Name the blood parasite species.
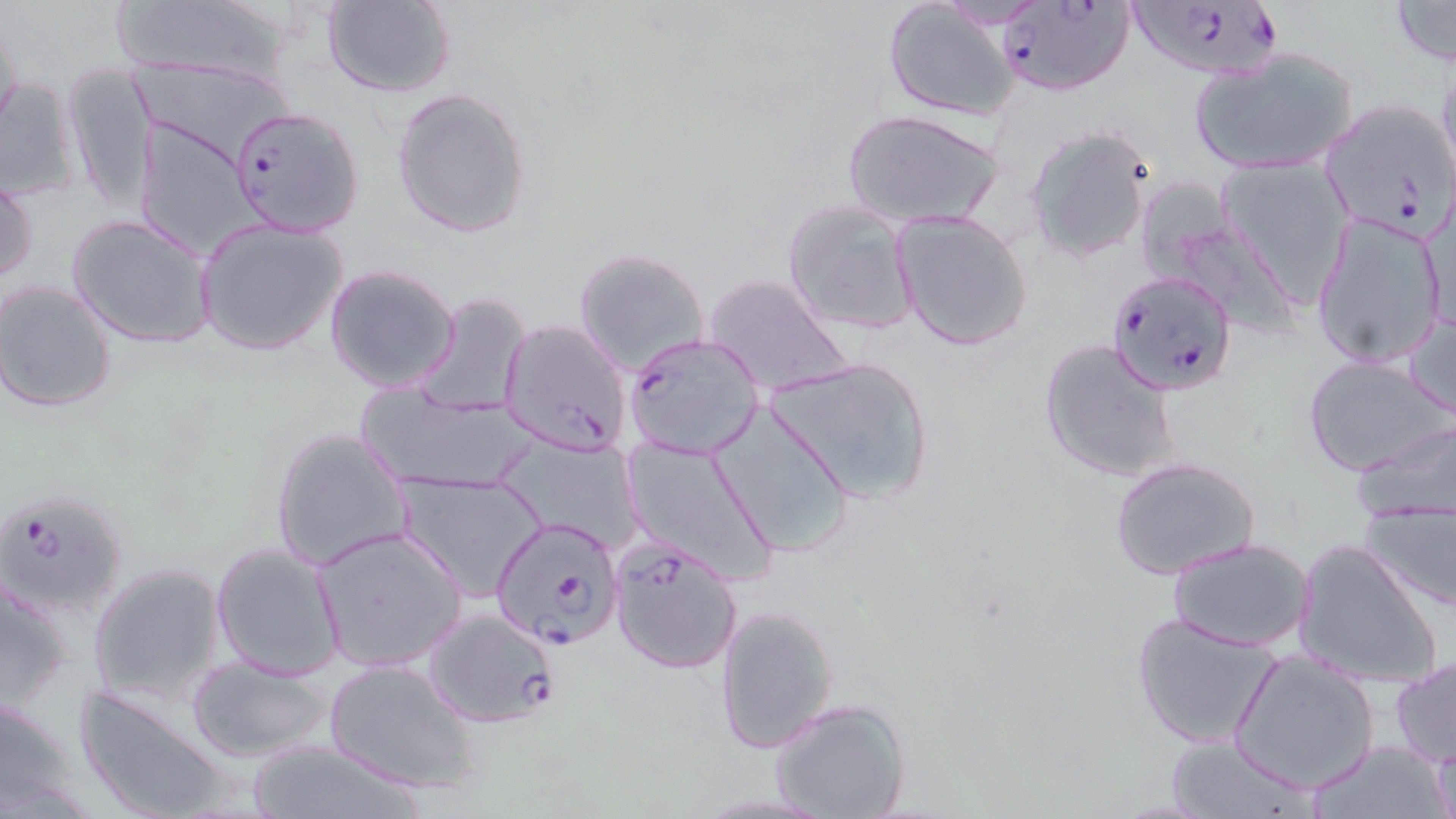

Plasmodium falciparum.

Summary:
  - Coordinate format: approximate bounding boxes as (x1, y1, x2, y2) in pixels
  - Uninfected red blood cell locations: (321, 0, 457, 99), (881, 0, 1024, 121), (1387, 0, 1456, 67), (108, 2, 292, 85), (0, 9, 24, 135), (1190, 44, 1361, 176), (129, 58, 296, 164), (1435, 59, 1456, 190), (62, 66, 158, 214), (0, 77, 87, 202), (392, 87, 532, 239), (842, 109, 1004, 230), (133, 123, 262, 258), (1023, 126, 1155, 264), (1215, 156, 1354, 299), (1, 170, 38, 292), (782, 198, 920, 336), (892, 210, 1033, 353), (69, 213, 217, 349), (1311, 213, 1448, 370), (195, 218, 349, 355), (574, 247, 709, 378), (324, 264, 462, 394), (701, 273, 851, 395), (1, 281, 120, 414), (413, 291, 532, 419), (1405, 306, 1455, 421), (1039, 338, 1179, 483), (1302, 354, 1452, 477), (766, 355, 934, 505), (355, 385, 539, 494), (711, 402, 857, 562), (1354, 418, 1456, 522), (269, 425, 413, 574), (497, 435, 644, 554), (623, 437, 778, 583), (1110, 457, 1261, 579), (395, 471, 547, 602), (1360, 501, 1456, 612), (311, 526, 468, 674), (1168, 536, 1318, 653), (1292, 539, 1445, 690), (210, 542, 345, 680), (88, 563, 226, 708), (0, 572, 75, 718), (716, 602, 840, 754), (1130, 612, 1281, 748), (1230, 650, 1380, 793), (187, 657, 336, 763), (1390, 657, 1456, 768), (325, 658, 483, 795), (73, 683, 235, 819), (0, 692, 88, 819), (770, 697, 909, 819), (1162, 733, 1316, 818), (240, 737, 432, 819), (1426, 737, 1454, 819), (1299, 738, 1454, 818)
  - Plasmodium falciparum-infected red blood cell locations: (1124, 0, 1291, 83), (997, 2, 1132, 96), (1318, 98, 1456, 241), (228, 103, 364, 238), (1105, 268, 1239, 395), (499, 318, 633, 457), (621, 331, 768, 462), (0, 488, 128, 620), (491, 516, 625, 650), (608, 535, 744, 676), (422, 608, 563, 728)
  - Stain: May-Grünwald-Giemsa
  - Preparation: thin blood smear
  - Field of view: single
  - Modality: light microscopy
  - Image size: 1456×819 pixels
  - Magnification: 1000x